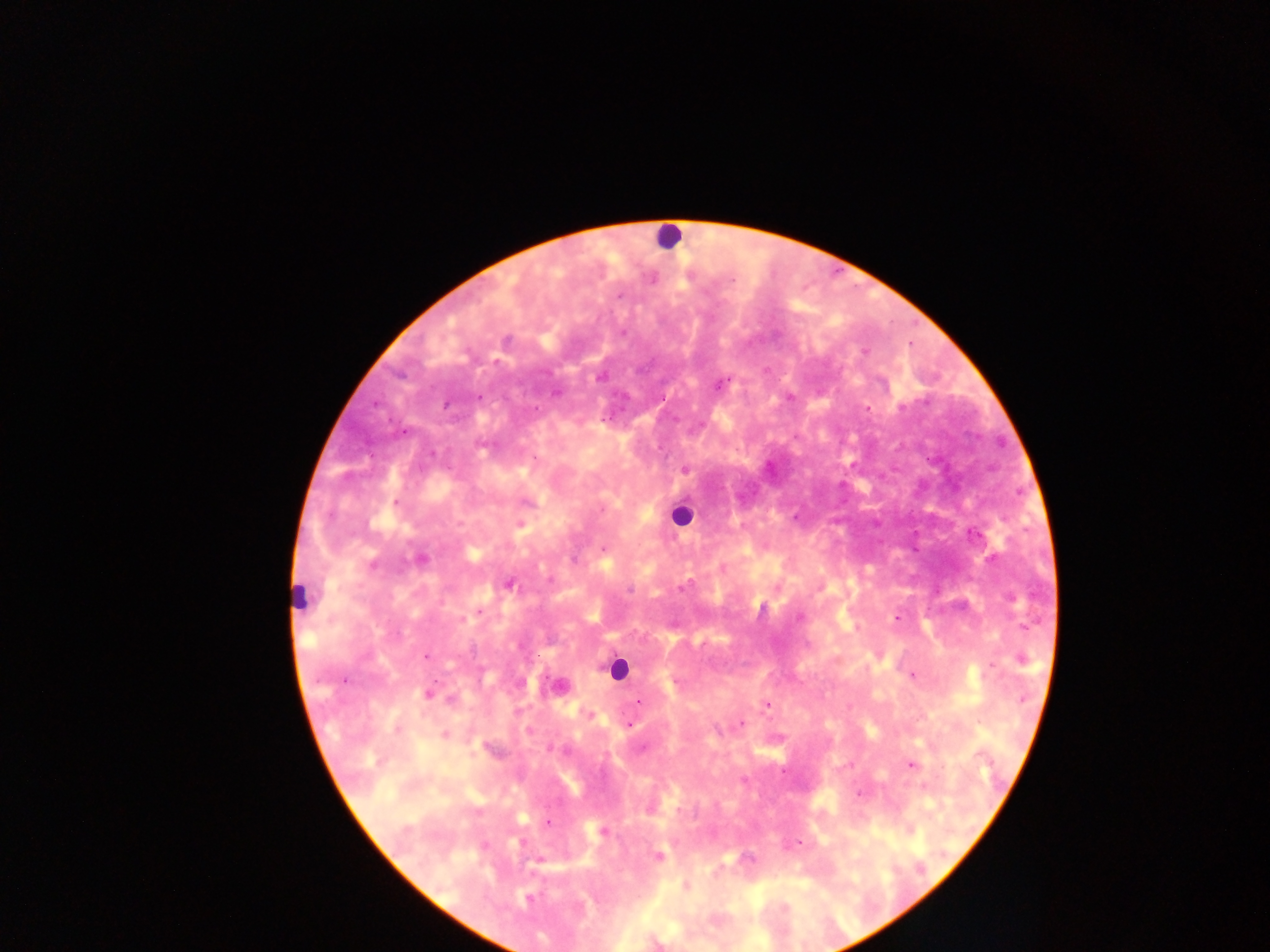 Approximate centers as [x, y] in pixels. Leukocyte locations: [667, 235], [680, 515], [299, 597], [616, 669]. Plasmodium parasite locations: [651, 278], [620, 295], [506, 341], [864, 351], [601, 376], [720, 383], [556, 391], [789, 397], [867, 408], [685, 468], [795, 517], [520, 525], [973, 534], [603, 550], [420, 558], [509, 584], [681, 587], [630, 589], [799, 616], [897, 618], [426, 655], [1020, 659], [912, 675], [558, 686], [428, 693], [639, 701], [767, 704], [590, 715], [739, 724], [629, 725], [444, 735], [643, 747], [911, 764], [925, 786], [859, 793], [649, 807], [547, 823], [602, 831], [796, 843], [657, 857], [685, 886], [527, 898]. Thick blood smear. Single field of view. Sample from Ghana. Photographed through a microscope with a mobile-phone camera. Image is 1270×952 pixels.